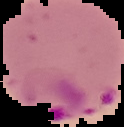

Image is 124×127 pixels. Cell region segmented out of the field of view; the surrounding area is masked to black. Malaria status: parasitized. From a thin blood film.